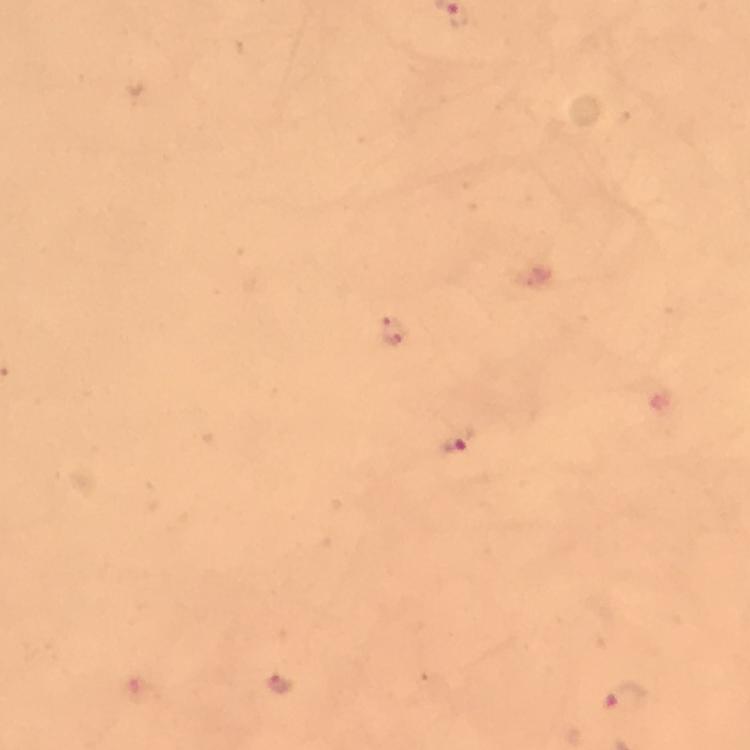

{
  "image_size": "750×750 pixels",
  "magnification": "100x",
  "stain": "Giemsa",
  "cropped_from": "a single field of view",
  "capture": "smartphone camera through the microscope",
  "immersion_oil": "used",
  "malaria_parasite_locations": "approximate centers as [x, y] in pixels: [394, 330], [457, 441], [283, 686], [629, 697]",
  "context": "from a malaria diagnostic workup",
  "preparation": "thick blood film"
}